Report the malaria status of this cell.
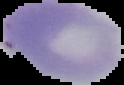

It is uninfected.

Summary:
  - Image size: 124×85 pixels
  - Image type: cell region segmented out of the field of view; surrounding area masked to black
  - Preparation: thin blood smear